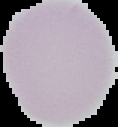

image type = segmented cell region with the area outside set to black
preparation = thin blood smear
image size = 118×127 pixels
result = negative for malaria parasites